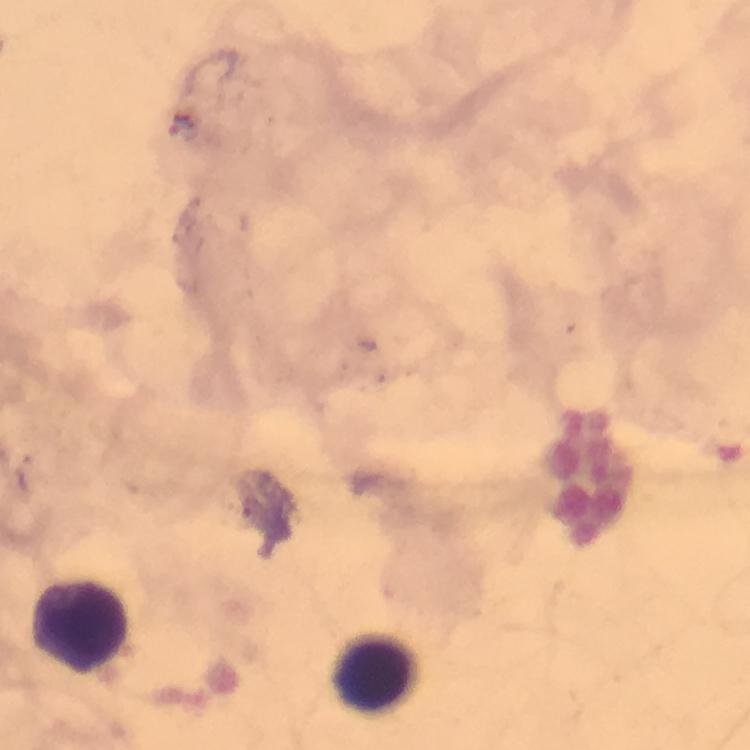

Approximate centers as (x, y) in pixels.
Summary:
  - Leukocyte locations: (79, 626), (374, 672)
  - Magnification: 100x
  - Stain: Giemsa
  - Capture: smartphone photograph through a microscope
  - Image size: 750×750 pixels
  - Immersion oil: applied
  - Preparation: thick smear
  - Cropped from: one field of view
  - Context: from a malaria diagnostic workup
  - Malaria parasites: none detected